Locate every leukocyte (white blood cell).
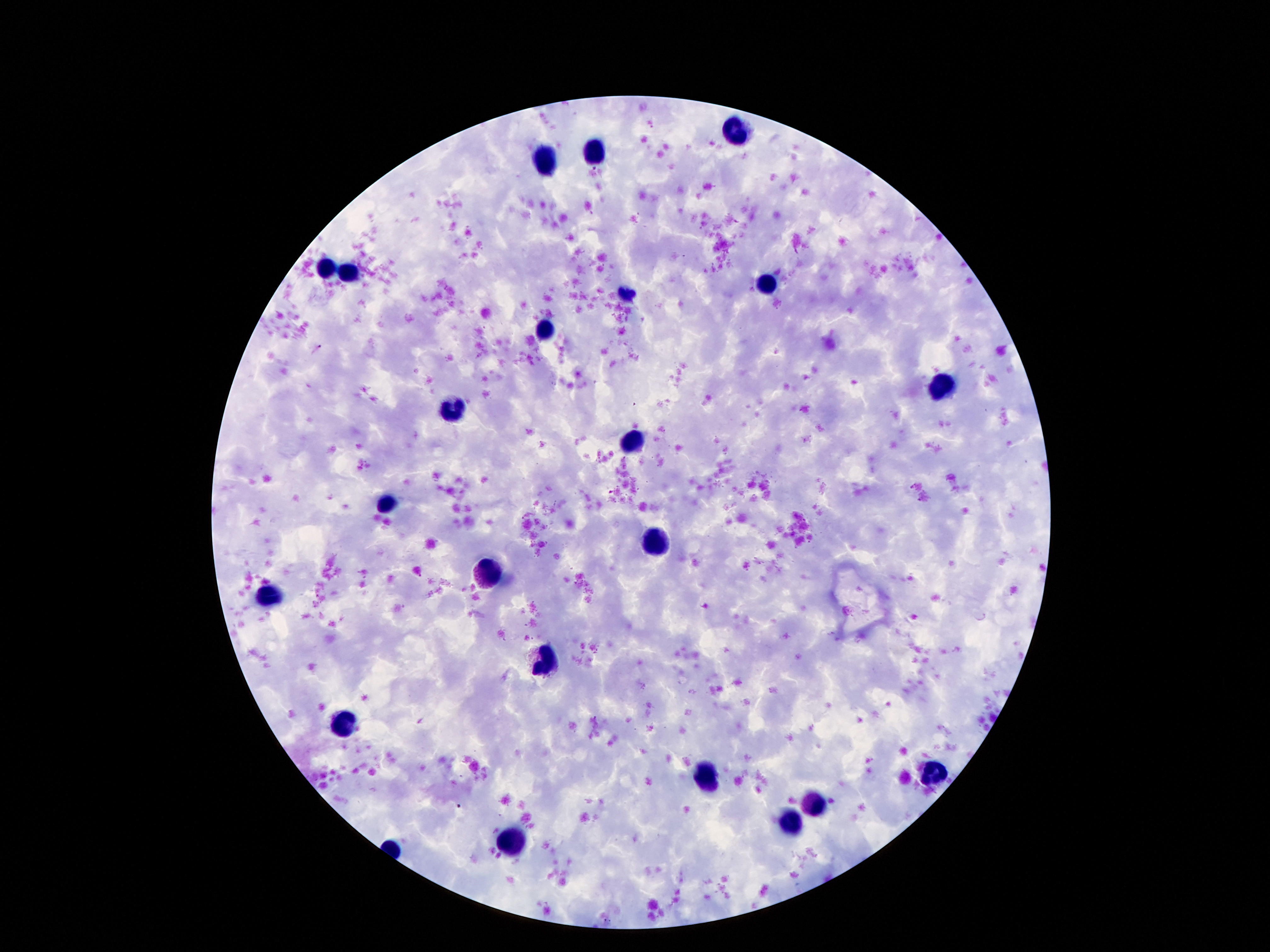
Approximate centers as (x, y) in pixels.
Leukocytes: (735, 128), (597, 154), (548, 163), (328, 267), (351, 271), (768, 284), (627, 293), (545, 330), (940, 388), (458, 409), (635, 442), (389, 501), (657, 542), (489, 576), (269, 596), (543, 661), (343, 721), (933, 775), (705, 778), (817, 804), (791, 824), (510, 836).

Summary:
  - Field of view: one from this slide
  - Patient malaria status: not infected
  - Stain: Giemsa
  - Image size: 1270×952 pixels
  - Preparation: thick blood film
  - Magnification: 100x
  - Capture: smartphone camera through the microscope eyepiece